Outline each blood parasite and name the species.
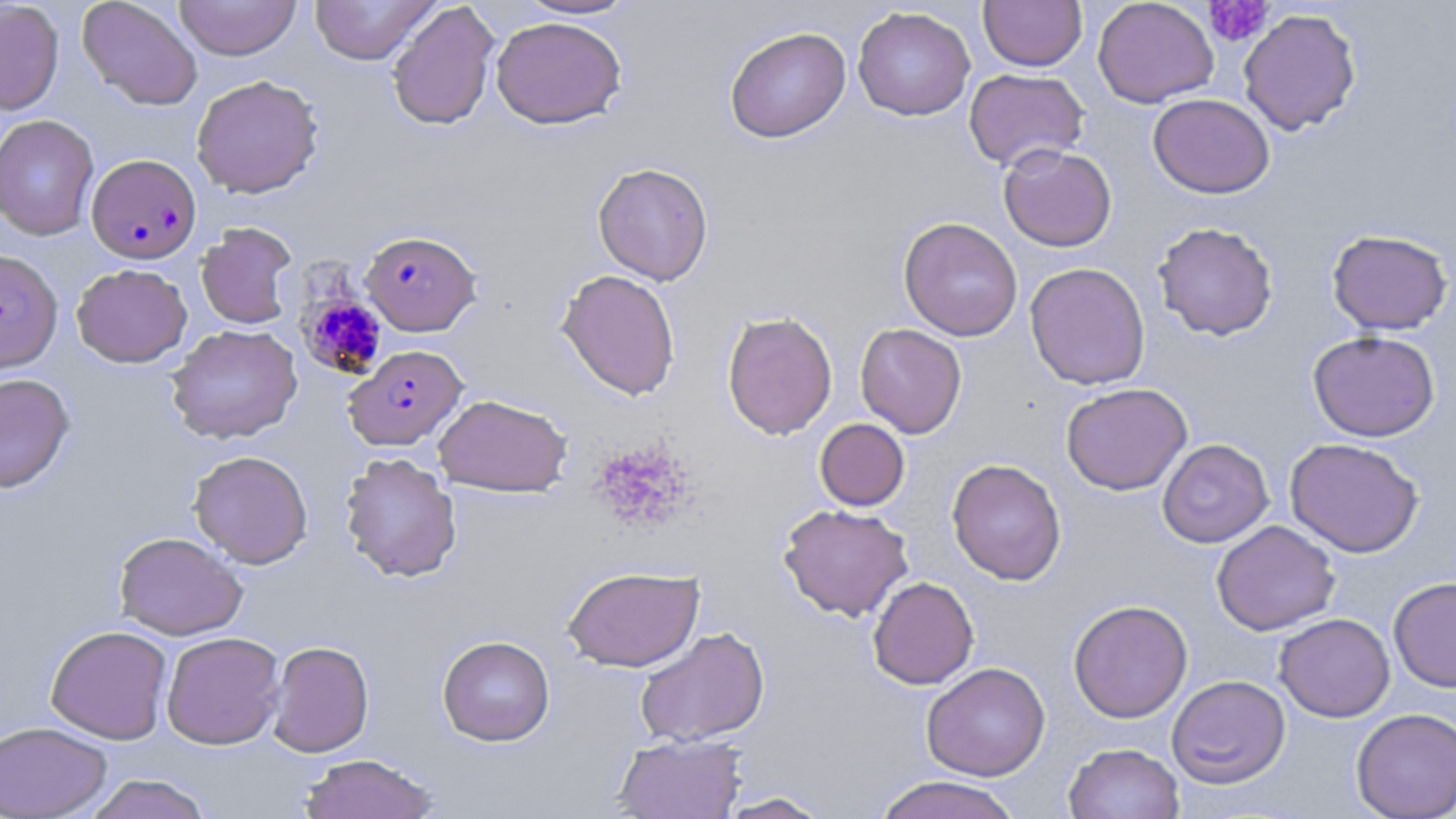
Approximate bounding boxes as [x1, y1, x2, y2] in pixels.
Plasmodium falciparum-infected red blood cells: [86, 154, 201, 264], [360, 230, 481, 336], [0, 248, 62, 374], [344, 344, 467, 450].
No Plasmodium ovale, Plasmodium malariae, Plasmodium vivax, Babesia divergens, or Trypanosoma brucei observed.

slide-level diagnosis = Plasmodium falciparum
modality = light microscopy
platelet locations = approximate bounding boxes as [x1, y1, x2, y2] in pixels: [1203, 1, 1274, 47], [296, 286, 389, 382], [591, 439, 696, 534]
magnification = 1000x
field of view = one of a larger specimen
preparation = thin blood smear
stain = May-Grünwald-Giemsa
image size = 1456×819 pixels
uninfected red blood cell locations = approximate bounding boxes as [x1, y1, x2, y2] in pixels: [77, 0, 203, 110], [174, 0, 301, 60], [309, 0, 441, 65], [516, 0, 639, 20], [979, 0, 1087, 72], [1092, 0, 1219, 108], [0, 1, 64, 115], [386, 1, 500, 131], [852, 6, 975, 121], [1238, 8, 1362, 136], [490, 16, 627, 129], [724, 26, 851, 143], [963, 68, 1089, 171], [191, 74, 324, 198], [1148, 93, 1275, 198], [0, 114, 100, 241], [998, 144, 1117, 252], [592, 162, 714, 286], [898, 216, 1023, 341], [1152, 221, 1278, 341], [196, 222, 298, 330], [1327, 229, 1453, 335], [1024, 261, 1150, 390], [71, 263, 192, 367], [556, 268, 681, 400], [721, 310, 838, 440], [855, 323, 967, 438], [166, 324, 303, 444], [1308, 330, 1440, 442], [0, 372, 75, 492], [1060, 382, 1192, 496], [434, 393, 572, 497], [814, 418, 910, 511], [1284, 437, 1424, 557], [1157, 439, 1274, 548], [188, 450, 313, 568], [339, 452, 462, 583], [947, 458, 1067, 585], [778, 503, 914, 622], [1211, 520, 1340, 636], [113, 531, 247, 640], [562, 565, 704, 672], [867, 576, 979, 689], [1388, 577, 1456, 692], [1068, 599, 1193, 724], [1274, 613, 1395, 722], [45, 625, 172, 744], [634, 626, 770, 747], [161, 631, 285, 750], [437, 635, 555, 746], [267, 640, 375, 758], [921, 662, 1050, 781], [1166, 674, 1290, 788], [1351, 707, 1456, 819], [0, 721, 112, 818], [612, 734, 747, 819], [1063, 742, 1184, 819], [298, 753, 440, 818], [84, 774, 213, 819], [873, 775, 1023, 819], [715, 791, 833, 818]